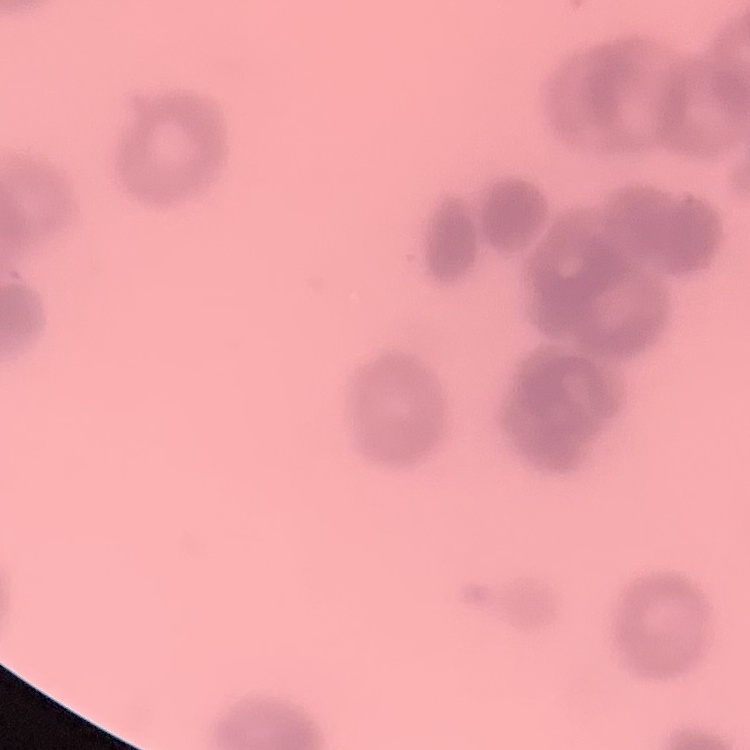
The red blood cells show rouleaux formation. Field's or Giemsa stain. One tile cut from a larger photomicrograph. Thin peripheral smear.